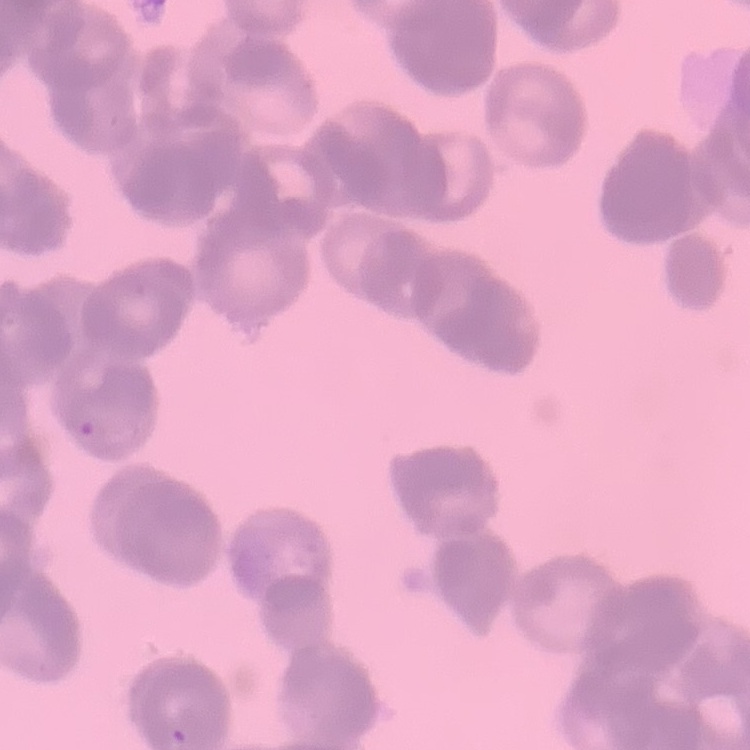
Summary:
  - Red blood cell morphology: rouleaux formation
  - Preparation: thin peripheral smear
  - Stain: Field's or Giemsa
  - Image type: one tile cut from a larger photomicrograph